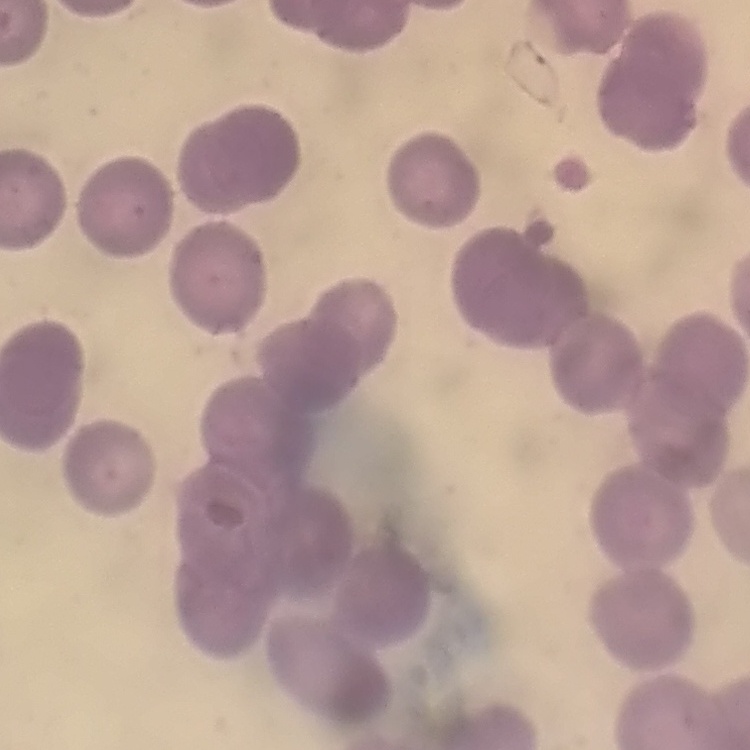
Summary:
  - Red blood cell morphology: no rouleaux formation
  - Stain: Field's or Giemsa
  - Image type: one tile cut from a larger photomicrograph
  - Preparation: thin peripheral smear